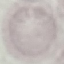
Malaria status: uninfected. Automatically extracted cell patch, resized to 64 × 64 pixels. Thin blood smear. Photographed with a smartphone camera at the microscope eyepiece. Giemsa stain.